Locate and identify every blood parasite.
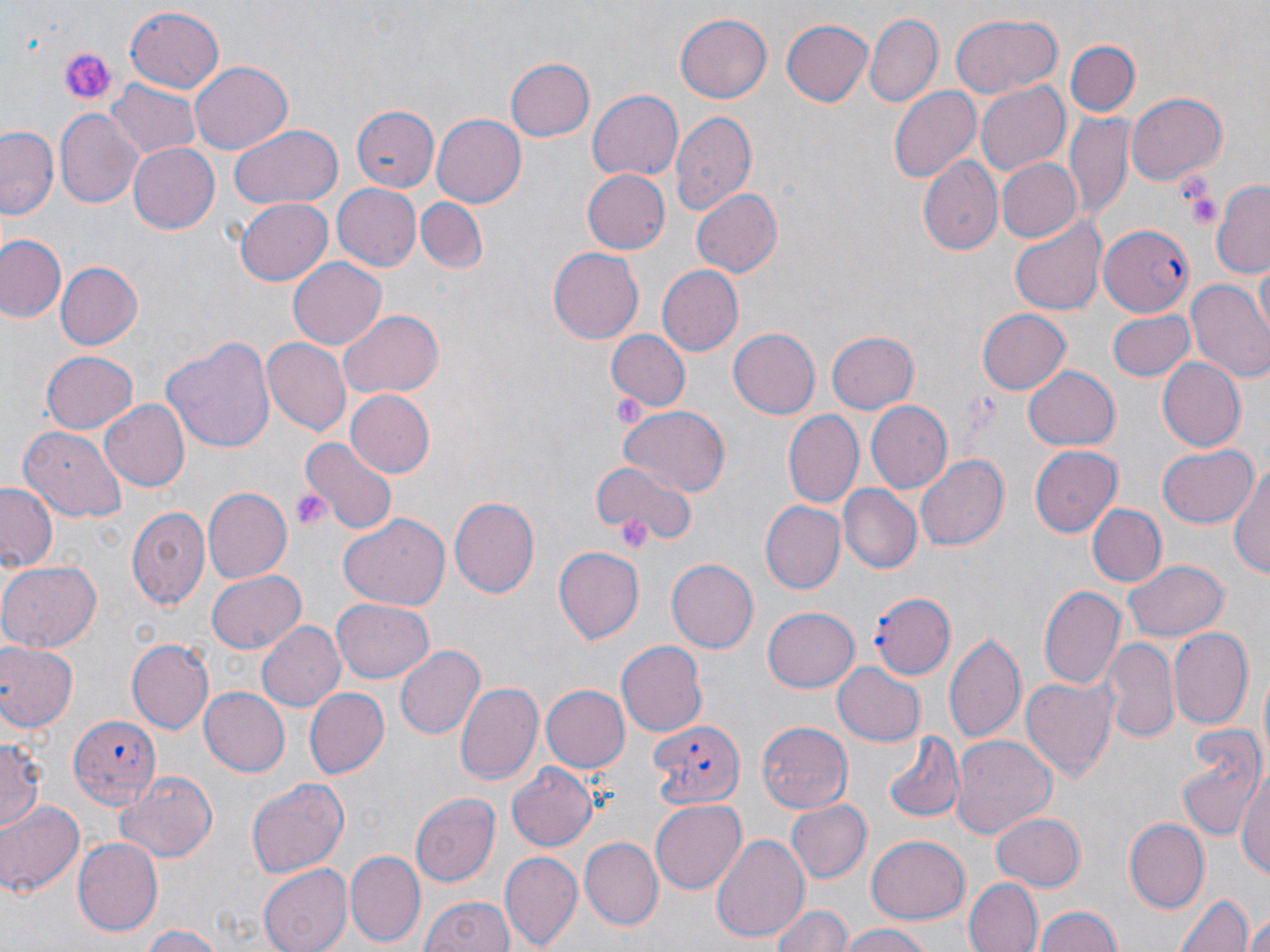

Approximate bounding boxes as (x1, y1, x2, y2) in pixels.
Plasmodium falciparum-infected red blood cells: (1098, 224, 1195, 316), (869, 589, 957, 677), (71, 716, 164, 806), (647, 719, 746, 810).
No Plasmodium ovale, Plasmodium malariae, Plasmodium vivax, Babesia divergens, or Trypanosoma brucei observed.

Summary:
  - Platelet locations: (56, 44, 118, 107), (1178, 179, 1221, 230), (609, 396, 649, 430), (289, 487, 332, 533), (614, 514, 650, 546)
  - Uninfected red blood cell locations: (123, 7, 227, 92), (673, 12, 771, 104), (865, 13, 942, 106), (950, 13, 1062, 96), (780, 18, 874, 106), (1064, 39, 1140, 116), (506, 59, 594, 142), (189, 61, 293, 155), (106, 79, 200, 158), (975, 81, 1070, 176), (889, 86, 982, 183), (587, 90, 685, 182), (1125, 92, 1228, 183), (350, 103, 439, 193), (56, 108, 144, 208), (670, 111, 757, 218), (431, 113, 526, 207), (1066, 114, 1134, 220), (230, 124, 342, 211), (1, 126, 60, 221), (128, 142, 219, 233), (918, 155, 1002, 255), (994, 157, 1083, 243), (582, 168, 671, 253), (1212, 180, 1270, 276), (330, 184, 421, 271), (689, 188, 783, 279), (414, 196, 489, 273), (234, 198, 334, 285), (1008, 218, 1105, 316), (1, 234, 64, 323), (547, 247, 643, 345), (1255, 256, 1269, 343), (288, 258, 387, 350), (55, 262, 144, 350), (659, 265, 746, 356), (1188, 280, 1270, 382), (977, 308, 1072, 392), (1106, 308, 1196, 381), (338, 310, 445, 397), (728, 327, 820, 418), (826, 329, 918, 414), (606, 330, 688, 410), (160, 333, 275, 455), (262, 339, 351, 436), (40, 351, 137, 434), (1157, 357, 1246, 451), (1023, 364, 1120, 449), (344, 389, 434, 478), (100, 399, 191, 492), (867, 399, 953, 493), (617, 404, 730, 495), (784, 413, 863, 507), (17, 426, 128, 520), (299, 437, 396, 534), (1029, 445, 1121, 538), (1154, 445, 1258, 528), (915, 454, 1007, 551), (1230, 454, 1270, 584), (591, 462, 692, 548), (0, 483, 60, 572), (838, 486, 922, 574), (201, 487, 291, 584), (452, 494, 540, 597), (758, 500, 846, 595), (125, 503, 210, 608), (1088, 504, 1165, 585), (339, 512, 451, 611), (553, 545, 643, 644), (1123, 558, 1228, 640), (0, 560, 102, 652), (667, 560, 757, 653), (205, 571, 307, 654), (1039, 585, 1125, 689), (332, 598, 435, 683), (763, 608, 859, 692), (257, 621, 346, 711), (1169, 626, 1255, 729), (944, 631, 1026, 744), (126, 637, 214, 735), (1102, 637, 1178, 743), (0, 640, 78, 734), (616, 640, 707, 737), (393, 645, 483, 742), (833, 662, 927, 744), (1022, 675, 1117, 780), (454, 681, 544, 788), (539, 685, 628, 773), (199, 687, 291, 776), (304, 688, 389, 779), (757, 721, 852, 812), (1175, 725, 1265, 842), (884, 734, 963, 822), (951, 734, 1056, 836), (0, 737, 42, 836), (505, 763, 595, 853), (1238, 764, 1269, 885), (115, 770, 217, 861), (247, 778, 348, 878), (411, 792, 499, 884), (650, 798, 746, 893), (787, 800, 872, 882), (0, 801, 83, 897), (988, 810, 1087, 892), (1122, 818, 1209, 913), (708, 831, 811, 946), (72, 836, 163, 932), (865, 836, 970, 923), (581, 838, 663, 928), (347, 851, 424, 945), (502, 852, 582, 948), (258, 864, 354, 952), (964, 877, 1041, 952), (1173, 889, 1255, 952), (419, 895, 513, 952), (772, 904, 852, 952), (1033, 905, 1122, 952), (1243, 916, 1270, 952), (835, 924, 937, 952), (140, 925, 224, 952)
  - Slide-level diagnosis: Plasmodium falciparum
  - Modality: light microscopy
  - Field of view: one of a larger specimen
  - Preparation: thin blood smear
  - Stain: May-Grünwald-Giemsa
  - Magnification: 1000x
  - Image size: 1270×952 pixels